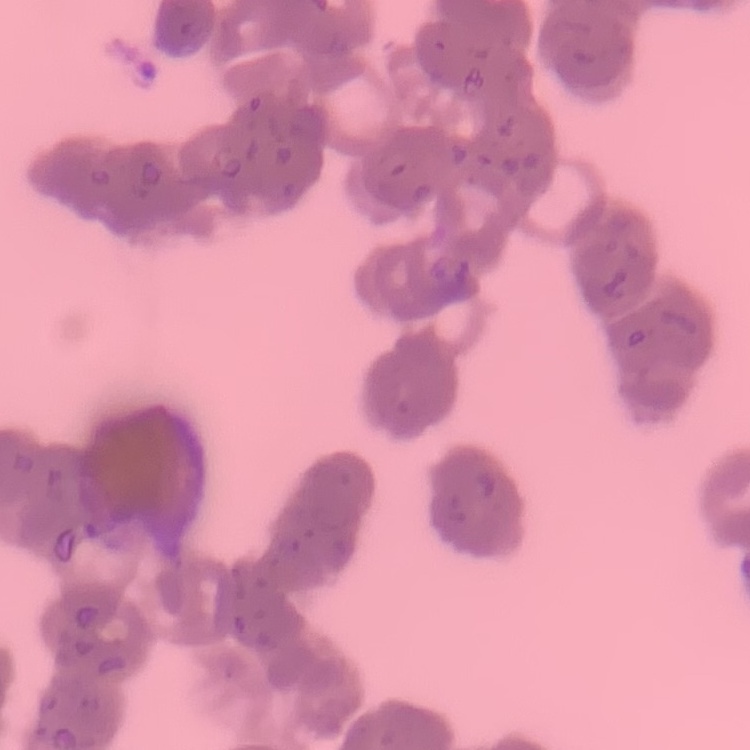

erythrocyte morphology = rouleaux formation
image type = square crop of a larger photomicrograph
preparation = thin blood film
stain = Field's or Giemsa